Give the extent of all Plasmodium ovale-infected red blood cells.
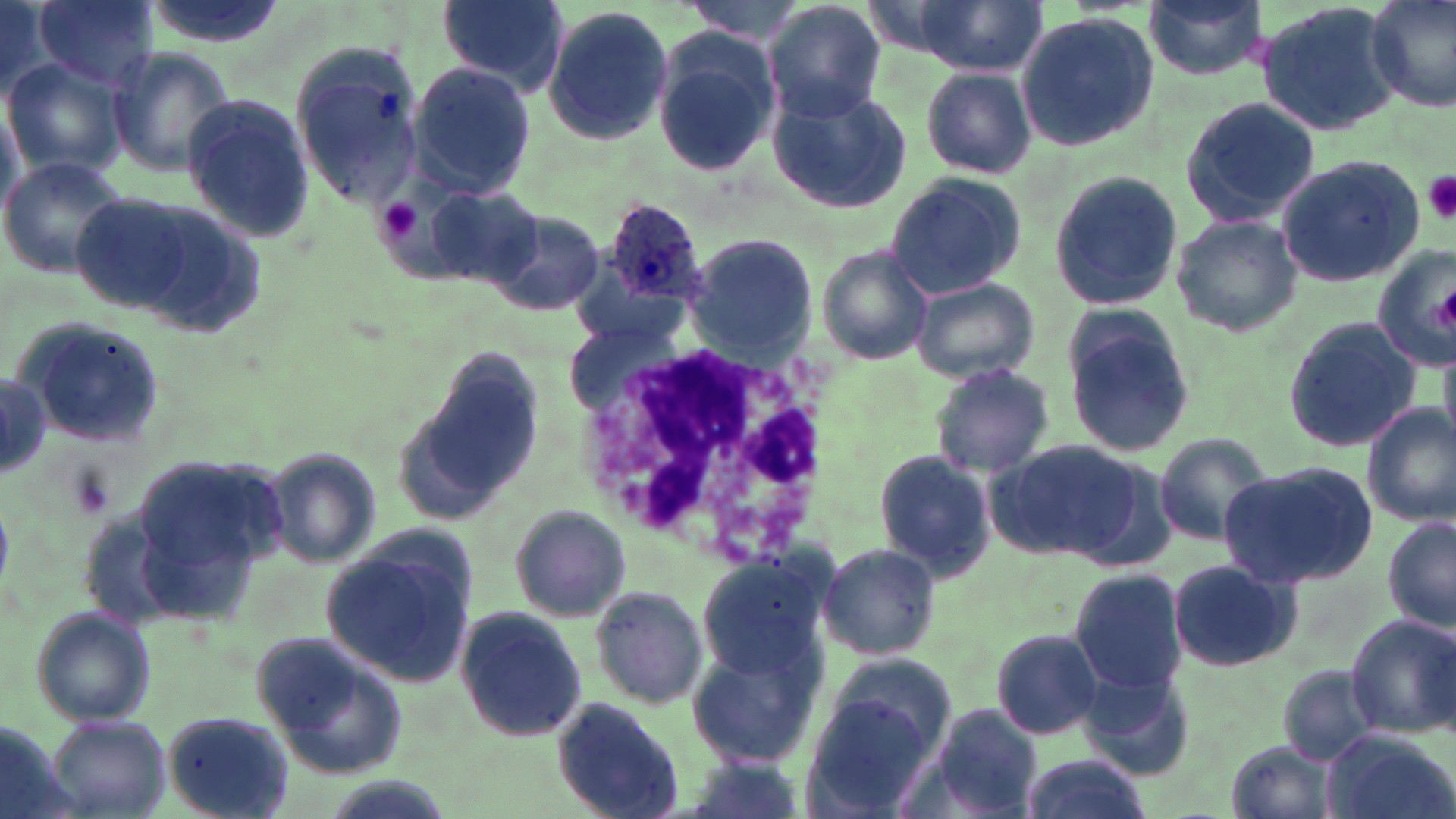
Approximate bounding boxes as (x1,y1)-(x2,y2) corner pairs in pixels.
Plasmodium ovale-infected red blood cells: (602,197)-(709,306).

slide-level diagnosis = Plasmodium ovale
stain = May-Grünwald-Giemsa
magnification = 1000x
preparation = thin blood smear
field of view = single
image size = 1456×819 pixels
white blood cell locations = approximate bounding boxes as (x1,y1)-(x2,y2) corner pairs in pixels: (576,341)-(833,560)
platelet locations = approximate bounding boxes as (x1,y1)-(x2,y2) corner pairs in pixels: (1423,172)-(1456,224), (374,198)-(425,245)
uninfected red blood cell locations = approximate bounding boxes as (x1,y1)-(x2,y2) corner pairs in pixels: (0,0)-(61,95), (35,0)-(157,91), (134,0)-(291,51), (912,0)-(1046,76), (1142,0)-(1268,81), (1365,0)-(1456,113), (439,1)-(570,92), (676,1)-(806,44), (1254,1)-(1405,139), (762,2)-(886,123), (542,7)-(674,145), (1014,11)-(1161,154), (651,31)-(779,176), (108,45)-(235,175), (289,46)-(425,206), (5,58)-(128,176), (407,61)-(536,199), (920,67)-(1038,178), (766,86)-(913,212), (180,94)-(313,243), (1178,94)-(1322,229), (0,98)-(27,215), (0,155)-(130,281), (1273,155)-(1425,287), (1049,168)-(1183,313), (883,172)-(1027,300), (427,187)-(543,288), (68,188)-(260,330), (483,205)-(605,317), (1170,212)-(1304,338), (684,235)-(815,363), (816,245)-(935,365), (1370,247)-(1455,374), (909,276)-(1040,385), (1057,305)-(1201,459), (1282,316)-(1424,454), (17,323)-(164,449), (406,348)-(551,518), (0,358)-(51,491), (930,361)-(1055,477), (1362,403)-(1456,526), (1152,433)-(1276,547), (993,439)-(1146,562), (260,447)-(379,569), (128,448)-(293,613), (875,449)-(994,578), (1219,462)-(1377,589), (0,503)-(12,590), (509,505)-(631,622), (1382,515)-(1455,636), (320,537)-(476,689), (816,542)-(944,662), (693,553)-(836,685), (1165,557)-(1303,675), (1068,570)-(1189,694), (588,584)-(708,713), (454,606)-(588,745), (34,607)-(154,730), (1346,614)-(1455,739), (991,628)-(1106,740), (257,636)-(411,780), (687,648)-(819,768), (823,654)-(956,760), (1276,662)-(1384,766), (1083,666)-(1197,780), (799,696)-(940,817), (551,698)-(685,819), (925,704)-(1045,819), (162,710)-(296,818), (45,715)-(172,817), (0,722)-(78,819), (1323,728)-(1455,819), (1226,738)-(1339,819), (679,752)-(811,819), (1016,753)-(1153,819)
modality = optical microscopy